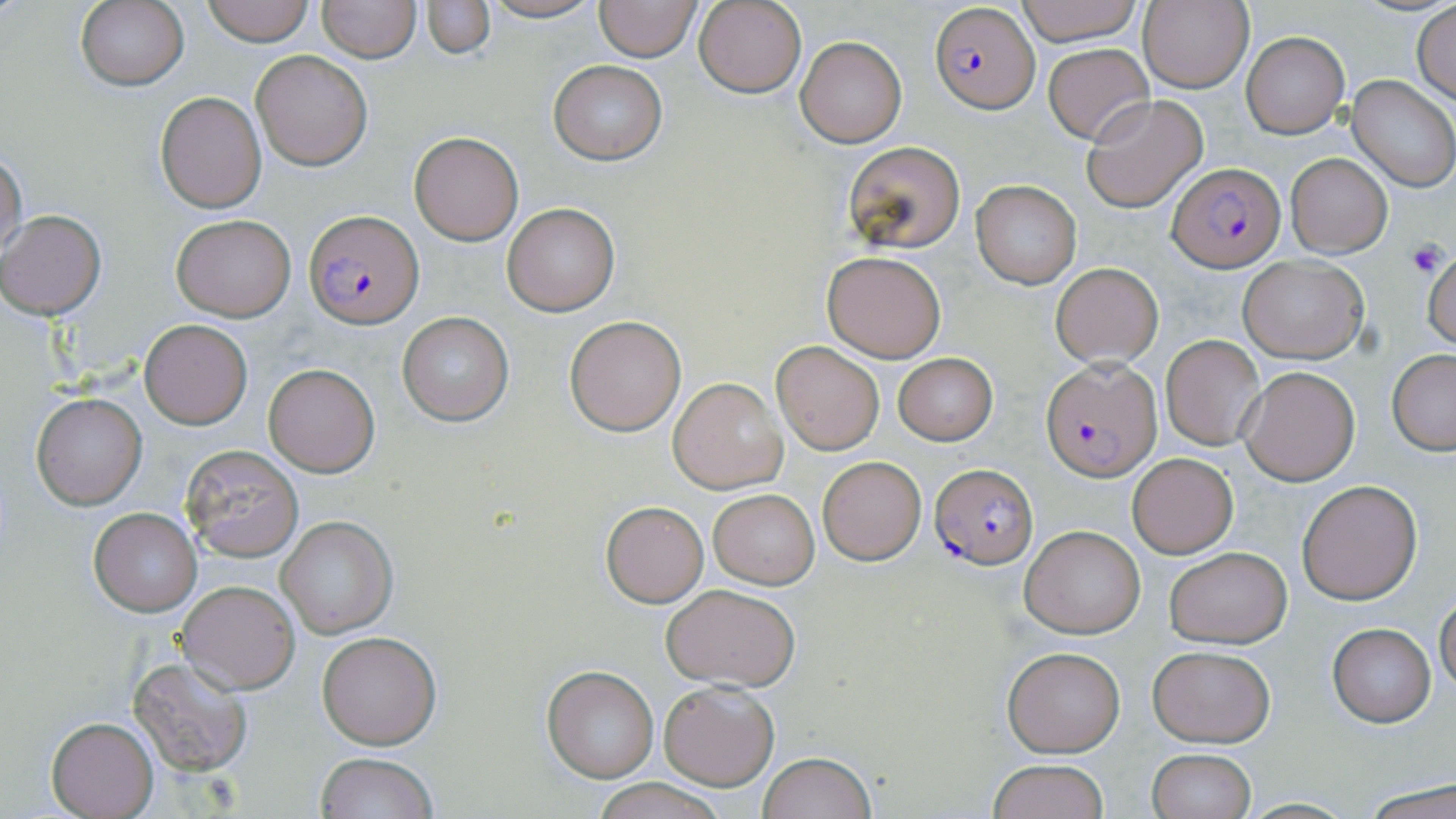

slide_level_diagnosis: Plasmodium falciparum
stain: May-Grünwald-Giemsa
magnification: 1000x
preparation: thin blood film
modality: optical microscopy
platelet_locations: 'approximate bounding boxes as (x1, y1, x2, y2) in pixels: (1406, 241, 1447, 278)'
plasmodium_falciparum_infected_red_blood_cell_locations: 'approximate bounding boxes as (x1, y1, x2, y2) in pixels: (930, 2, 1039, 112), (1171, 162, 1285, 271), (305, 210, 423, 327), (1042, 358, 1161, 480), (930, 462, 1039, 570)'
uninfected_red_blood_cell_locations: 'approximate bounding boxes as (x1, y1, x2, y2) in pixels: (75, 0, 188, 91), (203, 0, 315, 45), (474, 0, 606, 24), (592, 0, 703, 63), (1014, 0, 1146, 47), (1137, 0, 1254, 94), (319, 1, 419, 62), (422, 1, 494, 59), (694, 1, 806, 98), (1413, 4, 1456, 104), (1241, 32, 1349, 137), (796, 36, 906, 147), (1043, 43, 1153, 144), (251, 50, 374, 171), (548, 60, 667, 165), (1347, 75, 1456, 191), (155, 91, 267, 212), (1081, 95, 1208, 212), (409, 131, 524, 246), (841, 141, 967, 257), (0, 147, 27, 262), (1286, 153, 1392, 258), (970, 180, 1082, 289), (502, 203, 619, 316), (1, 210, 106, 318), (170, 214, 295, 321), (822, 249, 946, 362), (1421, 249, 1456, 350), (1237, 256, 1370, 364), (1051, 263, 1163, 368), (397, 313, 513, 425), (564, 315, 687, 436), (139, 319, 251, 428), (1161, 334, 1266, 451), (771, 340, 885, 454), (1388, 349, 1456, 454), (892, 353, 999, 446), (263, 363, 380, 476), (1239, 368, 1360, 484), (668, 377, 787, 493), (31, 391, 148, 510), (180, 445, 304, 563), (1127, 452, 1238, 558), (816, 455, 927, 566), (1295, 479, 1422, 605), (709, 490, 818, 589), (600, 500, 709, 607), (89, 507, 201, 616), (276, 516, 396, 638), (1020, 525, 1146, 638), (1164, 546, 1291, 647), (177, 580, 299, 694), (661, 583, 803, 692), (1435, 596, 1456, 696), (1327, 622, 1437, 728), (317, 632, 441, 748), (1147, 645, 1275, 747), (1002, 646, 1125, 757), (128, 654, 253, 774), (542, 666, 659, 782), (658, 680, 779, 788), (46, 717, 159, 818), (1146, 749, 1256, 819), (757, 750, 875, 819), (315, 752, 437, 819), (987, 758, 1110, 819), (588, 779, 733, 818), (1362, 781, 1456, 819)'
image_size: 1456×819 pixels
field_of_view: one of a larger specimen